Classify this cell by malaria status.
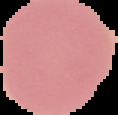
It is uninfected.

From a thin blood smear. Segmented cell region on a black background. Image is 118×115 pixels.